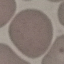

malaria status = uninfected
stain = Giemsa
image type = cell patch, automatically extracted from a larger field of view and resized to 64 × 64 pixels
capture = smartphone camera at the microscope eyepiece
preparation = thin blood smear